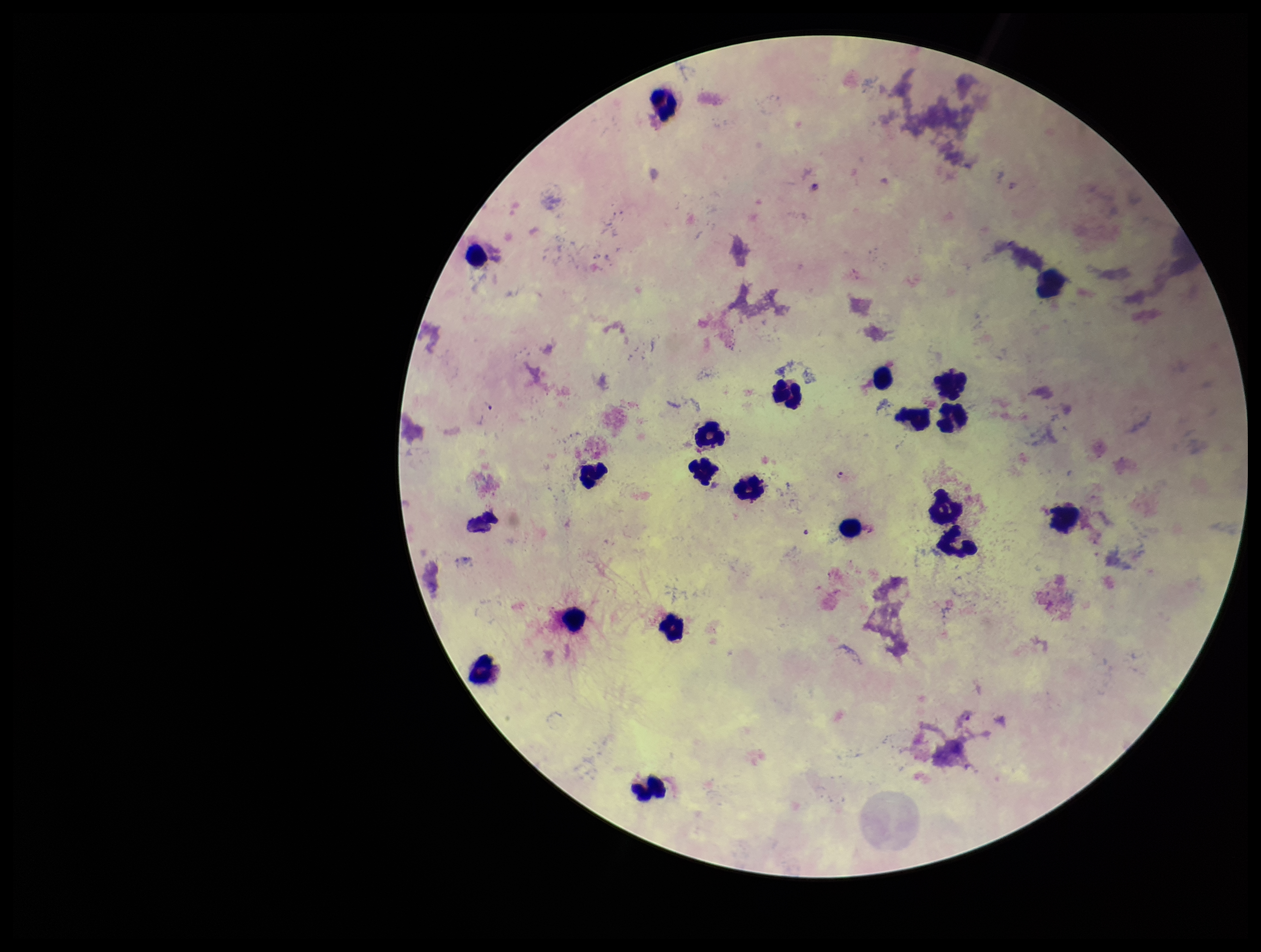

Summary:
  - Capture: smartphone photograph through the microscope eyepiece
  - Parasite count: 4
  - Stain: Giemsa
  - Preparation: thick
  - Field of view: one from this slide
  - Species reported for this patient: Plasmodium falciparum
  - Leukocyte count: 20
  - Patient malaria status: infected
  - Image size: 1261×952 pixels
  - Plasmodium parasites: seen